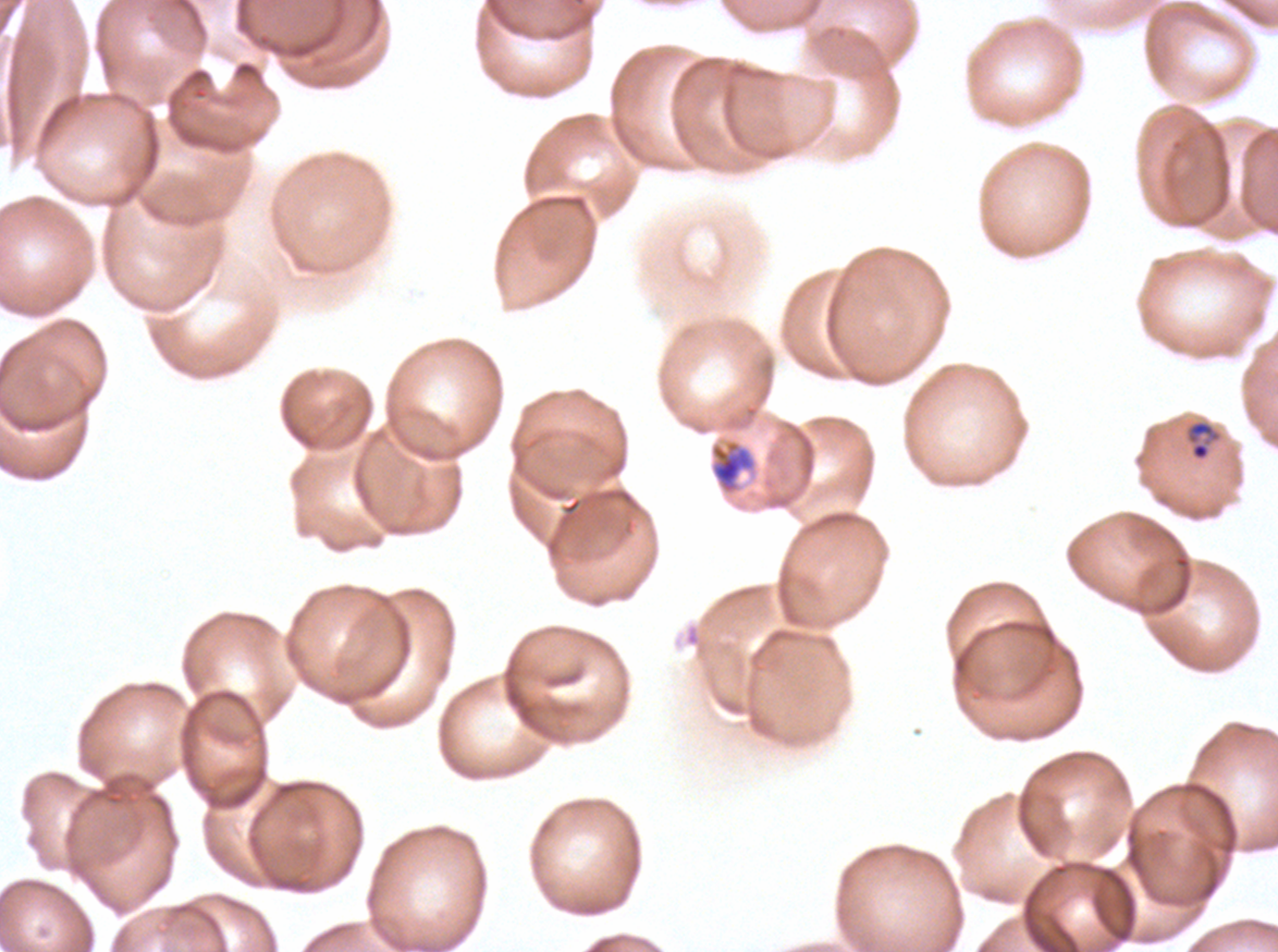

life_cycle_stages_observed: late-ring/early-trophozoite, mid trophozoite
late_ring_early_trophozoite_locations: 'approximate bounding boxes as [x1, y1, x2, y2] in pixels: [1185, 419, 1223, 462]'
preparation: thin blood smear
stain: Giemsa
image_size: 1278×952 pixels
field_of_view: one sub-image of a larger composite
specimen: ex-vivo P. falciparum culture from a patient in The Gambia, grown for 24 to 48 hours
mid_trophozoite_locations: 'approximate bounding boxes as [x1, y1, x2, y2] in pixels: [710, 441, 755, 494]'